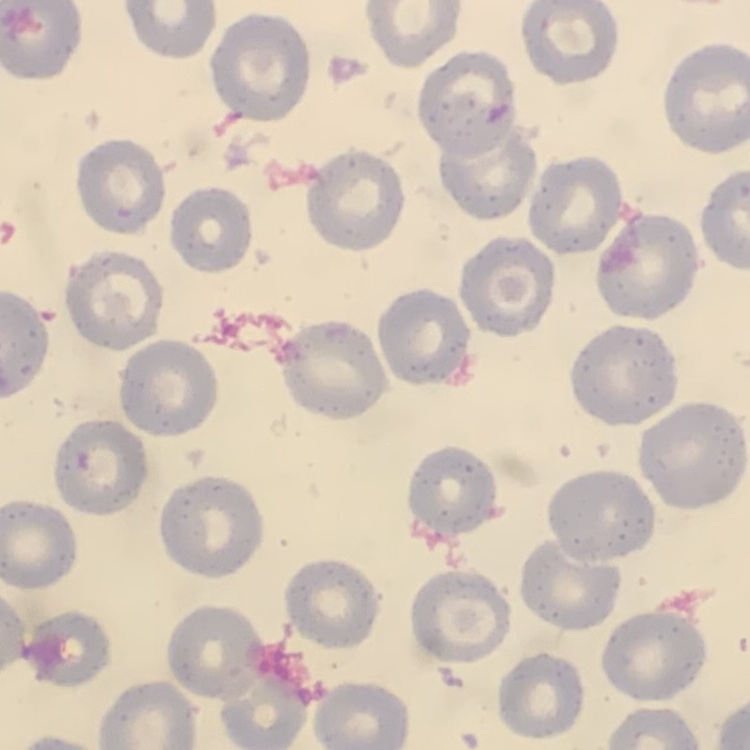

erythrocyte morphology = no rouleaux formation
image type = one tile cut from a larger photomicrograph
stain = Field's or Giemsa
preparation = thin blood smear